Name the parasite shown.
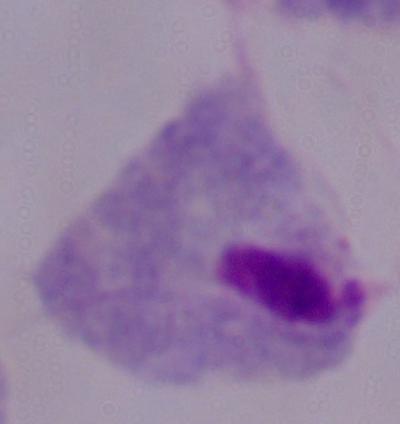

This is a trichomonad.

Photomicrograph. 1000x magnification.